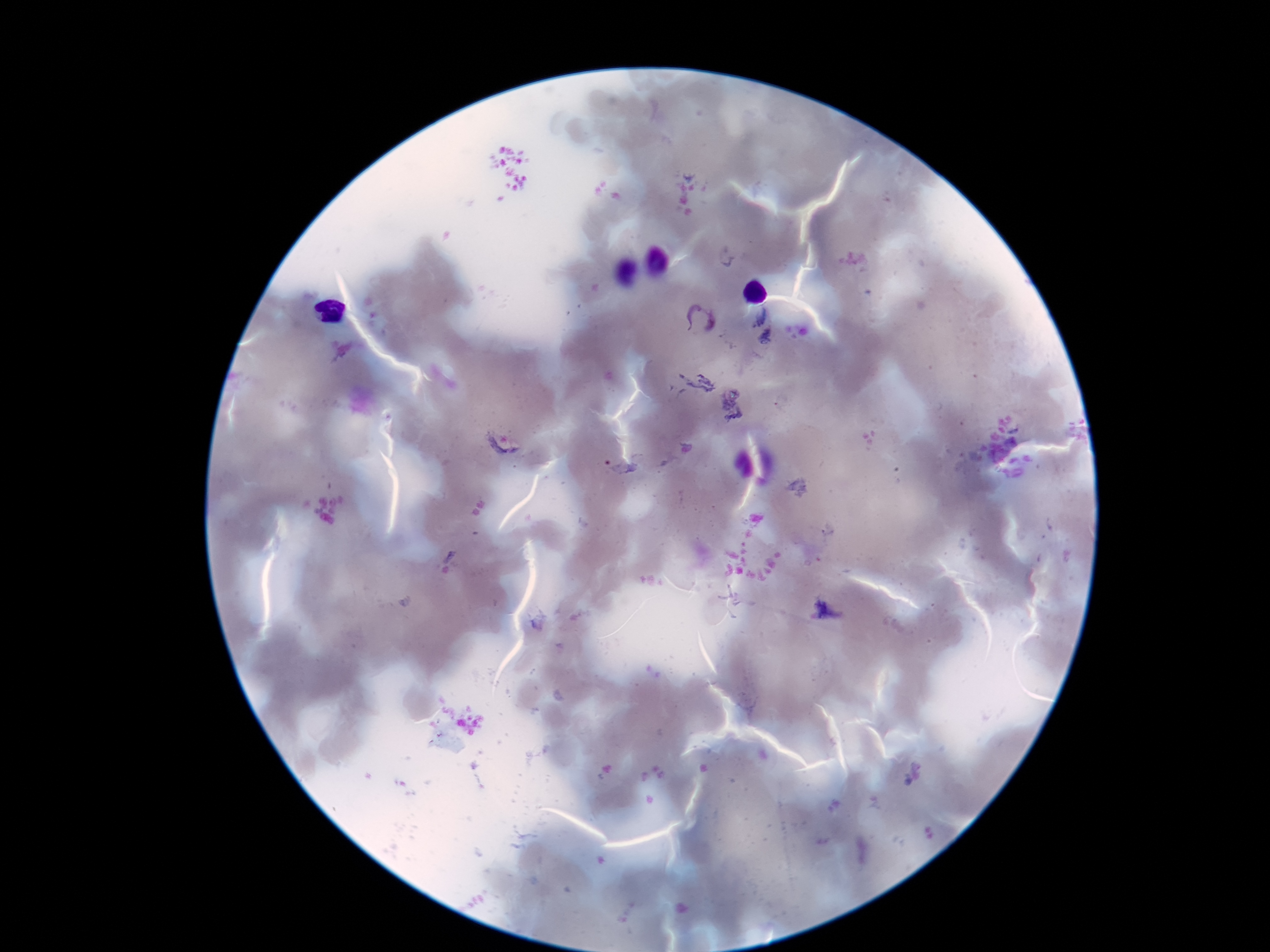
field of view = single
image size = 1270×952 pixels
capture = smartphone camera through the microscope eyepiece
Plasmodium parasite locations = approximate object centers, in pixels from the top-left corner: (x=758, y=315), (x=699, y=320), (x=765, y=338), (x=501, y=443), (x=620, y=470), (x=826, y=612)
stain = Giemsa
magnification = 100x
patient malaria status = infected
preparation = thick peripheral-blood smear